Identify the parasite.
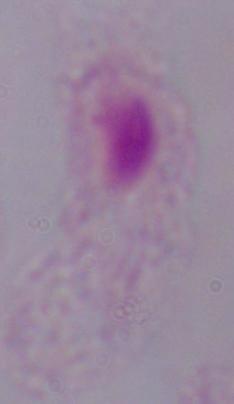
This is a trichomonad.

magnification = 1000x
modality = micrograph